Outline each P. falciparum parasite and classify it by life-cycle stage.
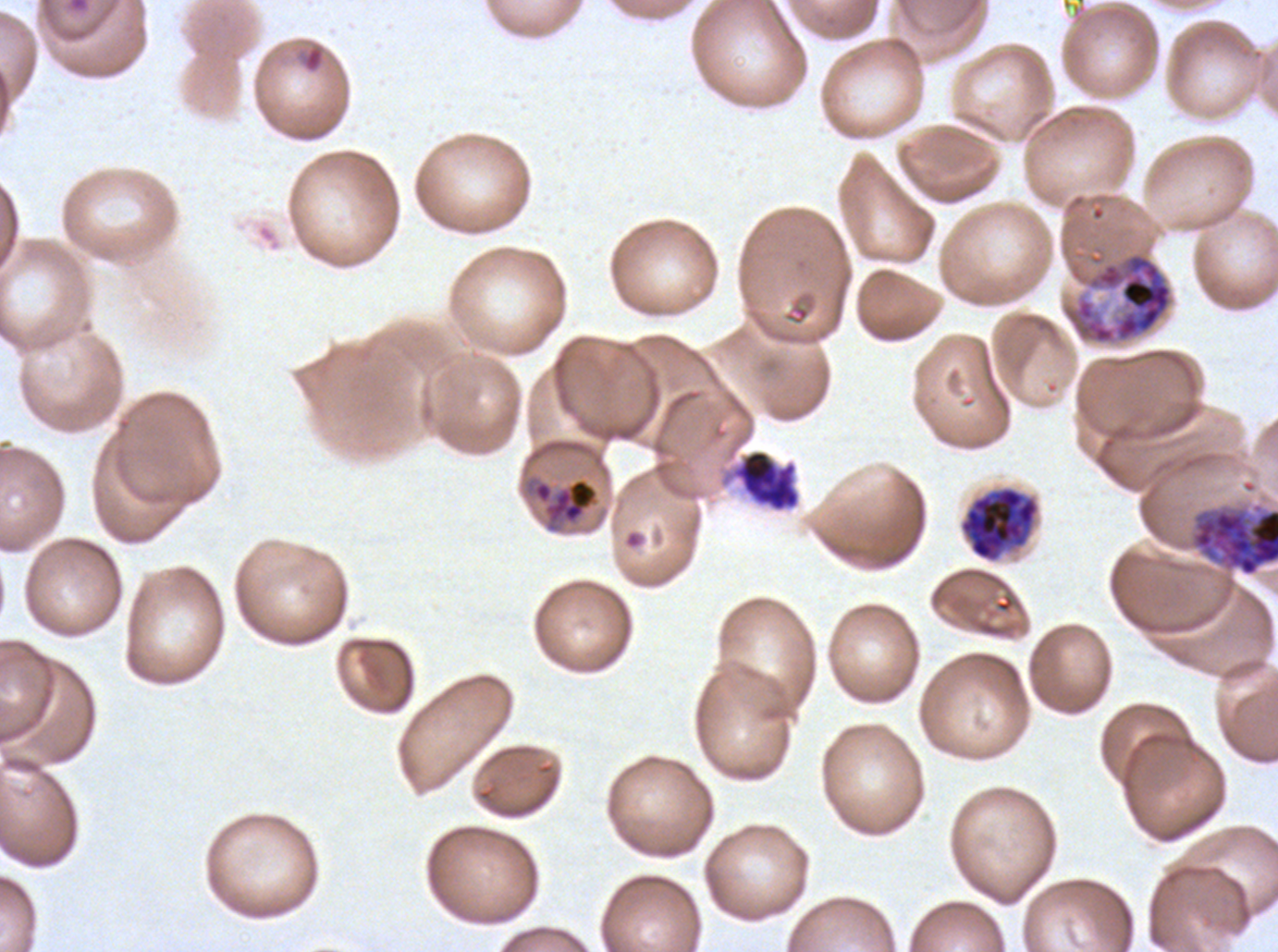

Approximate bounding boxes as {x1, y1, x2, y2} in pixels.
Rings: {304, 46, 323, 71}.
Mid trophozoites: {532, 477, 599, 532}.
Early schizonts: {1063, 250, 1174, 346}, {1188, 502, 1277, 578}.
Late schizonts: {960, 486, 1039, 562}.
Segmenters: {731, 449, 801, 512}.
No late-ring/early-trophozoite forms, late trophozoites, or gametocytes observed.

Summary:
  - Specimen: P. falciparum from a patient in The Gambia, cultured ex vivo for 24 to 48 hours
  - Image size: 1278×952 pixels
  - Preparation: thin blood film
  - Stain: Giemsa
  - Field of view: sub-image separated from a larger composite
  - Life-cycle stages observed: ring, mid trophozoite, early schizont, late schizont, segmenter